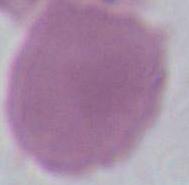
Summary:
  - Identification: erythrocyte
  - Modality: photomicrograph
  - Magnification: 1000x